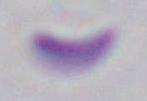
modality = micrograph
identification = Toxoplasma gondii
magnification = 1000x